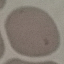
Summary:
  - Result: no malaria parasites detected
  - Capture: smartphone through the microscope eyepiece
  - Stain: Giemsa
  - Image type: automatically extracted cell patch, resized to 64 × 64 pixels
  - Preparation: thin blood film